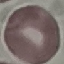

Summary:
  - Malaria status: uninfected
  - Image type: automatically extracted cell patch, resized to 64 × 64 pixels
  - Preparation: thin smear
  - Capture: smartphone camera at the microscope eyepiece
  - Stain: Giemsa